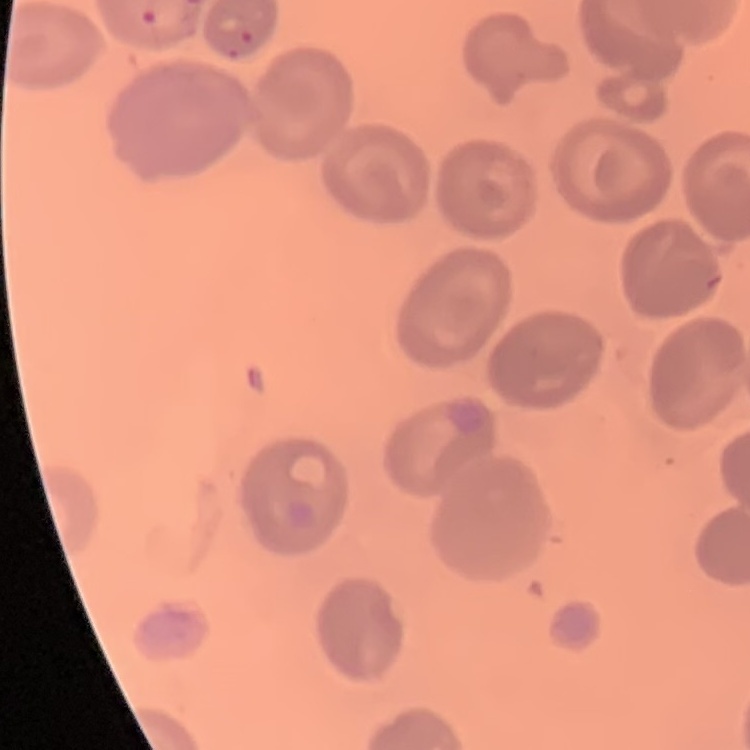

red_blood_cell_morphology: no rouleaux formation
image_type: square crop of a larger photomicrograph
preparation: thin blood film
stain: Field's or Giemsa